State the blood parasite species.
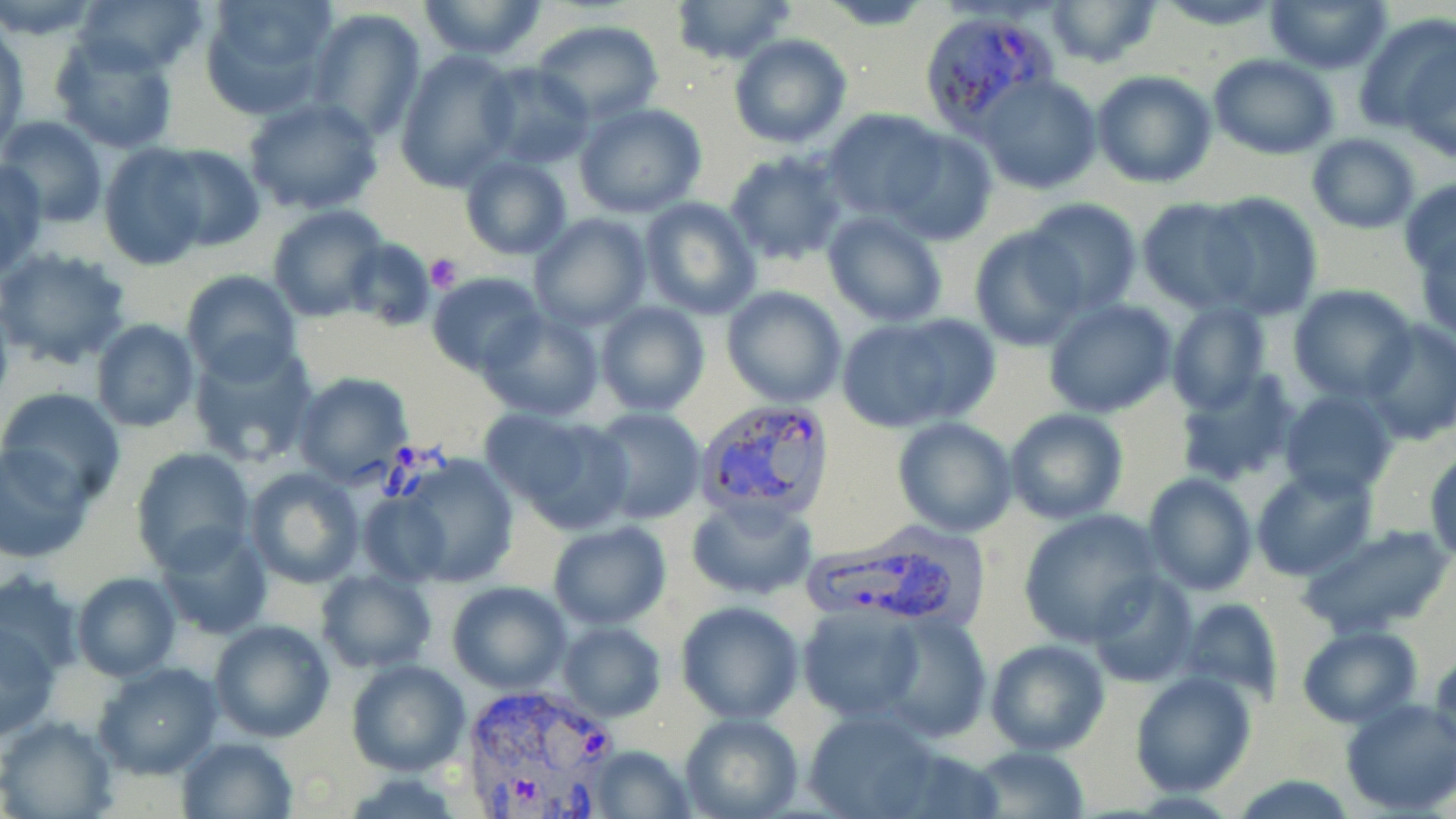
Plasmodium vivax.

Approximate bounding boxes as (x1, y1, x2, y2) in pixels. Uninfected red blood cell locations: (0, 0, 103, 39), (73, 0, 207, 76), (197, 0, 341, 119), (416, 0, 550, 61), (816, 0, 938, 30), (1045, 0, 1160, 70), (1150, 0, 1287, 30), (1266, 0, 1393, 72), (668, 1, 798, 66), (307, 8, 426, 139), (1357, 12, 1455, 136), (533, 20, 662, 124), (1, 27, 28, 149), (49, 34, 180, 156), (728, 34, 851, 148), (1402, 45, 1456, 162), (397, 48, 520, 190), (1208, 54, 1339, 159), (478, 64, 596, 168), (1091, 70, 1216, 188), (978, 74, 1102, 196), (243, 96, 383, 214), (575, 103, 707, 218), (822, 110, 948, 221), (3, 116, 106, 226), (884, 128, 998, 246), (1305, 133, 1422, 234), (97, 145, 210, 268), (153, 146, 263, 251), (725, 148, 849, 267), (459, 154, 572, 259), (0, 160, 48, 276), (1399, 179, 1456, 280), (1199, 192, 1323, 319), (639, 197, 761, 319), (1021, 198, 1142, 317), (1135, 198, 1256, 312), (267, 205, 388, 321), (822, 210, 948, 327), (530, 213, 651, 332), (967, 227, 1087, 350), (340, 239, 437, 330), (1, 247, 133, 370), (182, 270, 301, 383), (427, 272, 545, 374), (1289, 286, 1418, 402), (721, 287, 848, 406), (1044, 300, 1178, 418), (595, 301, 709, 417), (1166, 302, 1271, 414), (477, 311, 604, 422), (861, 314, 1000, 426), (1362, 319, 1456, 445), (91, 321, 199, 432), (186, 340, 318, 469), (1175, 368, 1300, 489), (294, 373, 413, 487), (0, 387, 125, 507), (1280, 390, 1397, 502), (588, 408, 706, 526), (1004, 409, 1128, 524), (504, 412, 636, 533), (891, 416, 1018, 537), (0, 442, 96, 563), (132, 447, 255, 571), (1428, 449, 1456, 565), (386, 454, 519, 589), (1250, 466, 1380, 581), (244, 467, 364, 588), (1141, 472, 1257, 596), (354, 485, 457, 587), (686, 494, 819, 601), (1018, 510, 1160, 646), (1300, 521, 1451, 639), (548, 522, 671, 630), (154, 524, 272, 638), (316, 568, 436, 672), (1088, 569, 1200, 687), (0, 573, 82, 683), (71, 573, 181, 681), (447, 581, 571, 694), (1180, 596, 1283, 706), (675, 600, 805, 724), (797, 605, 925, 722), (878, 610, 991, 743), (209, 618, 335, 743), (2, 622, 59, 740), (557, 622, 667, 722), (1297, 625, 1420, 728), (984, 638, 1110, 756), (346, 659, 470, 774), (94, 663, 223, 779), (1130, 670, 1256, 796), (1339, 699, 1456, 814), (800, 708, 946, 819), (679, 713, 802, 819), (0, 716, 116, 818), (178, 736, 297, 819), (582, 745, 694, 818), (971, 747, 1091, 818), (1230, 775, 1361, 817). Platelet locations: (423, 255, 463, 292). Plasmodium vivax-infected red blood cell locations: (918, 9, 1054, 135), (698, 396, 835, 525), (802, 527, 983, 634), (455, 680, 621, 817). Thin blood film. May-Grünwald-Giemsa stain. Image is 1456×819 pixels. Optical microscopy. Captured at 1000x magnification. Single field of view.